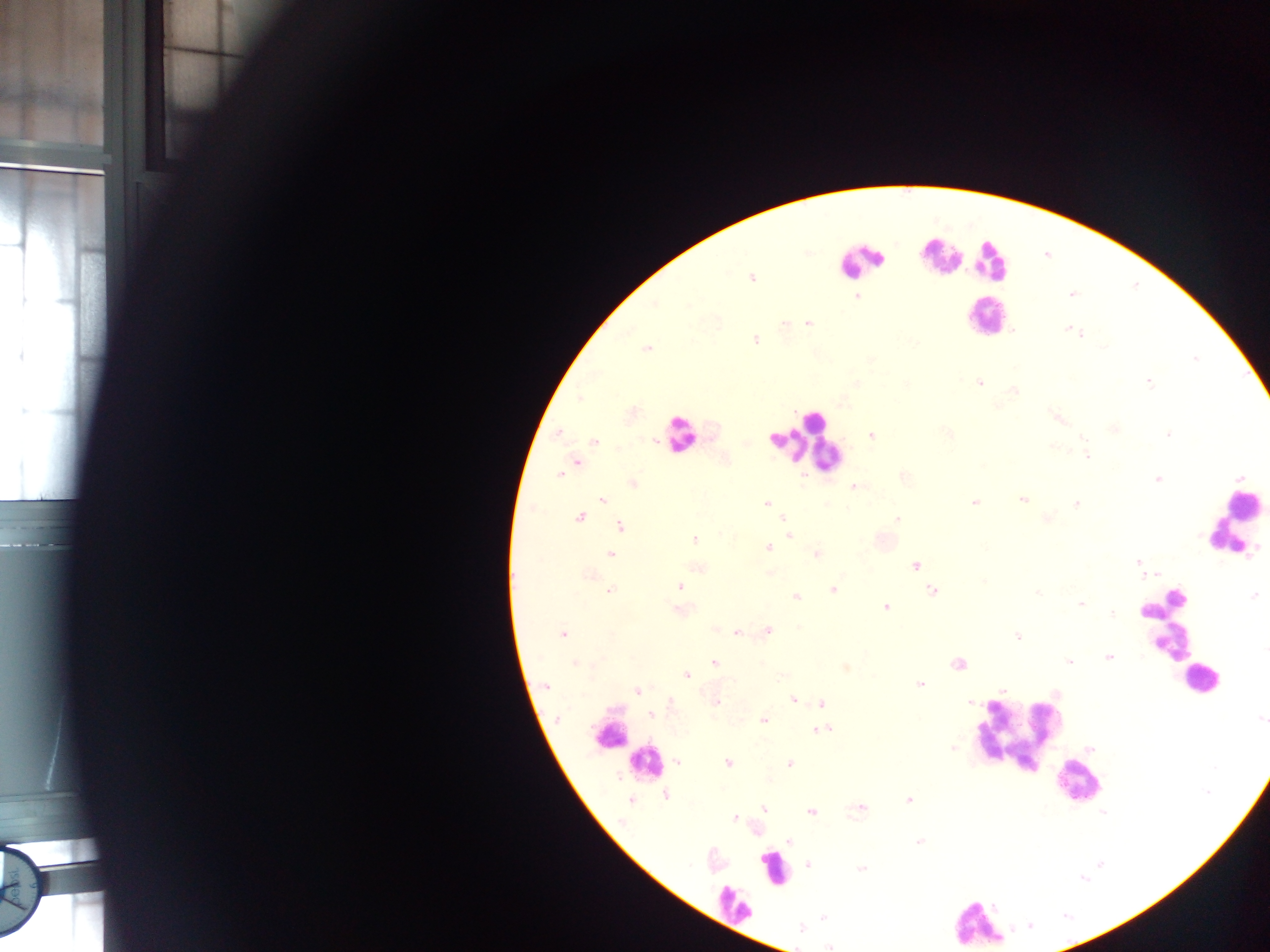 Approximate centers as (x, y) in pixels. Plasmodium parasite locations: (751, 278), (1071, 294), (857, 296), (808, 323), (784, 324), (1068, 328), (1079, 333), (755, 339), (647, 349), (979, 382), (1149, 382), (857, 383), (1013, 391), (579, 397), (843, 403), (1056, 417), (1113, 429), (558, 433), (948, 434), (872, 435), (1169, 435), (655, 440), (594, 442), (1051, 447), (1087, 456), (576, 462), (558, 474), (1158, 478), (633, 482), (853, 486), (602, 499), (1022, 499), (974, 502), (766, 504), (1077, 504), (580, 517), (1048, 518), (783, 519), (897, 519), (620, 527), (789, 535), (694, 540), (768, 548), (610, 554), (816, 554), (1138, 562), (915, 565), (770, 573), (588, 575), (679, 587), (833, 589), (609, 591), (932, 592), (1037, 593), (796, 596), (1253, 596), (1080, 603), (885, 606), (679, 610), (1113, 614), (768, 630), (737, 633), (563, 634), (1017, 637), (1265, 648), (1108, 657), (1069, 662), (714, 663), (957, 663), (575, 664), (845, 667), (686, 675), (782, 675), (920, 684), (546, 686), (1002, 689), (637, 690), (794, 700), (716, 702), (971, 702), (671, 703), (821, 703), (651, 715), (557, 719), (1260, 719), (764, 720), (822, 730), (952, 747), (678, 763), (728, 763), (790, 763), (666, 795), (908, 799), (631, 800), (860, 808), (764, 809), (811, 811), (735, 817), (790, 842), (919, 842), (808, 865), (861, 869), (823, 917), (801, 928), (829, 946). Leukocyte locations: (940, 256), (989, 260), (860, 261), (983, 317), (681, 435), (801, 442), (1240, 505), (1169, 624), (1198, 681), (1019, 732), (606, 736), (644, 761), (1075, 783), (773, 867), (733, 904), (978, 924). Image is 1270×952 pixels. Photographed through a microscope with a mobile-phone camera. Collected in Ghana. Thick blood smear. Single field of view.